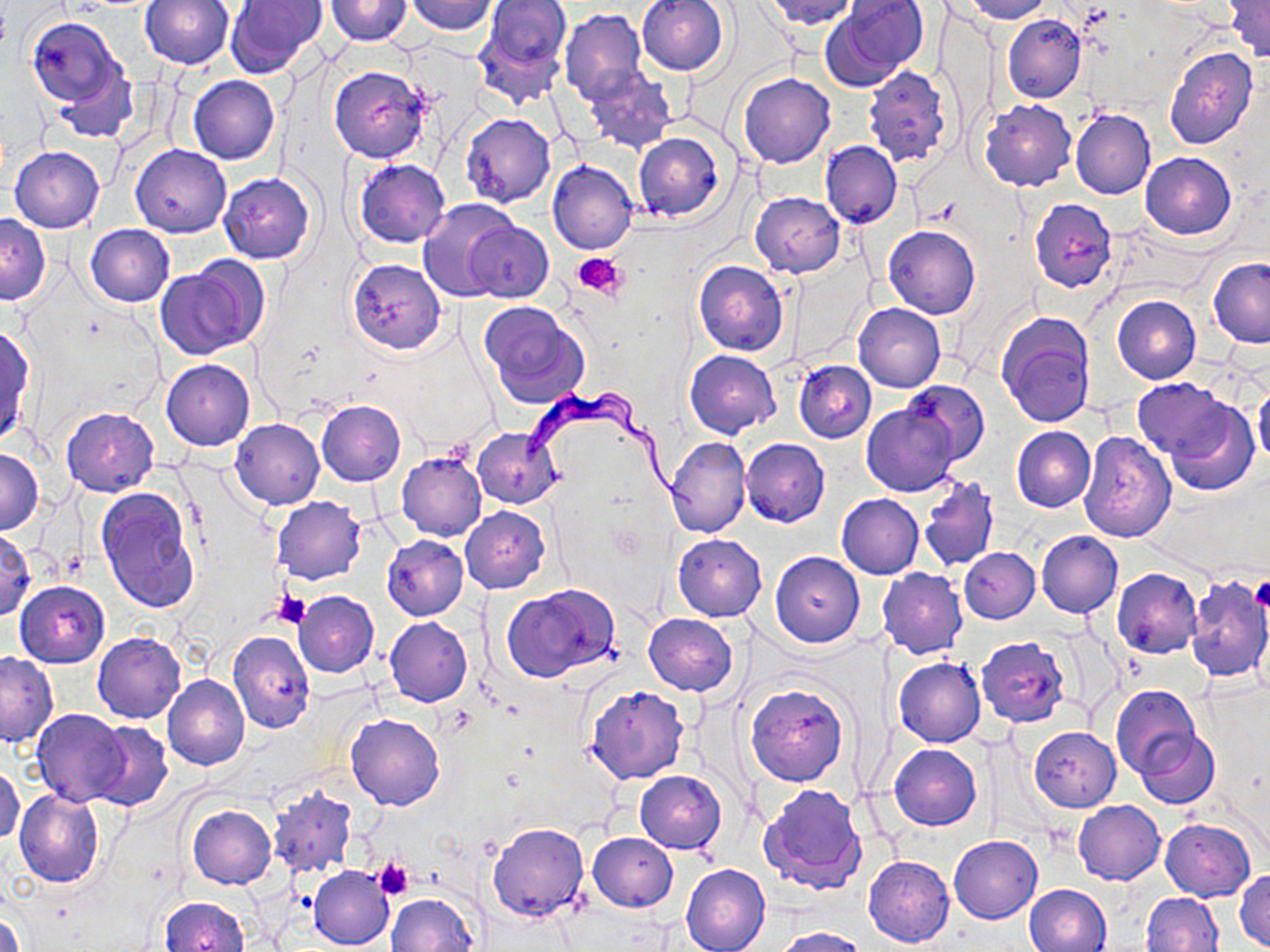
Approximate bounding boxes as (x1, y1, x2, y2) in pixels. Trypanosoma brucei locations: (522, 387, 703, 520). Uninfected red blood cell locations: (225, 0, 328, 79), (324, 0, 413, 45), (761, 0, 859, 30), (827, 0, 928, 85), (964, 0, 1052, 22), (140, 1, 233, 70), (405, 1, 496, 35), (481, 1, 571, 74), (636, 1, 731, 76), (1223, 1, 1270, 61), (560, 9, 647, 105), (1003, 14, 1085, 103), (994, 15, 1080, 186), (28, 18, 125, 109), (473, 21, 567, 111), (1164, 47, 1258, 151), (50, 62, 139, 145), (328, 65, 431, 163), (583, 66, 677, 155), (863, 66, 953, 167), (738, 73, 835, 168), (188, 75, 279, 166), (979, 100, 1076, 191), (1070, 110, 1156, 200), (460, 113, 556, 208), (633, 132, 725, 222), (821, 141, 902, 229), (132, 143, 231, 238), (9, 145, 105, 232), (1139, 151, 1236, 238), (354, 158, 451, 248), (547, 160, 638, 256), (219, 172, 315, 264), (750, 192, 845, 277), (418, 198, 518, 302), (1029, 198, 1117, 293), (1, 215, 49, 303), (464, 222, 554, 301), (86, 224, 173, 307), (884, 225, 980, 319), (1208, 258, 1270, 348), (347, 259, 446, 353), (693, 260, 790, 355), (156, 263, 260, 360), (1112, 296, 1200, 384), (479, 303, 590, 408), (855, 303, 945, 392), (997, 312, 1097, 428), (0, 326, 35, 446), (685, 349, 780, 437), (161, 359, 254, 450), (794, 360, 877, 442), (1134, 378, 1229, 463), (899, 379, 989, 464), (1254, 383, 1270, 468), (1162, 398, 1259, 496), (317, 401, 406, 485), (863, 403, 959, 496), (61, 407, 159, 496), (231, 419, 324, 508), (1012, 427, 1096, 512), (471, 428, 562, 508), (1077, 431, 1176, 542), (665, 436, 751, 538), (740, 438, 829, 527), (0, 448, 43, 533), (396, 452, 486, 541), (919, 476, 999, 571), (95, 488, 200, 613), (836, 494, 923, 579), (272, 495, 367, 585), (460, 507, 550, 594), (1036, 530, 1122, 618), (0, 532, 35, 620), (673, 534, 766, 621), (381, 535, 468, 620), (959, 547, 1039, 623), (770, 552, 865, 647), (878, 569, 967, 659), (1111, 569, 1202, 658), (1185, 576, 1270, 684), (15, 581, 109, 668), (501, 584, 622, 684), (293, 591, 379, 677), (644, 613, 737, 695), (384, 617, 472, 706), (227, 630, 314, 734), (93, 632, 185, 722), (975, 636, 1071, 728), (1, 652, 57, 746), (893, 657, 985, 747), (164, 676, 250, 771), (747, 683, 846, 786), (585, 685, 689, 784), (1111, 686, 1200, 777), (31, 709, 129, 807), (345, 713, 445, 810), (87, 721, 173, 811), (1029, 727, 1120, 811), (1135, 729, 1219, 809), (888, 744, 981, 830), (1, 761, 24, 846), (635, 771, 726, 854), (268, 785, 358, 879), (760, 785, 867, 895), (16, 789, 104, 887), (1074, 800, 1164, 884), (186, 805, 276, 889), (1161, 818, 1255, 901), (487, 822, 588, 922), (588, 832, 677, 912), (949, 835, 1042, 924), (864, 855, 954, 947), (682, 863, 769, 952), (309, 865, 394, 949), (1234, 869, 1270, 950), (306, 881, 476, 950), (1023, 884, 1111, 952), (386, 891, 479, 952), (1141, 892, 1225, 952), (158, 897, 249, 952), (1, 908, 26, 952), (770, 927, 869, 951). Platelet locations: (574, 252, 628, 301), (1249, 578, 1270, 614), (274, 591, 312, 630), (374, 859, 413, 899). Slide-level diagnosis: Trypanosoma brucei. Single field of view. Image is 1270×952 pixels. Thin blood film. Light microscopy. 1000x magnification. May-Grünwald-Giemsa stain.